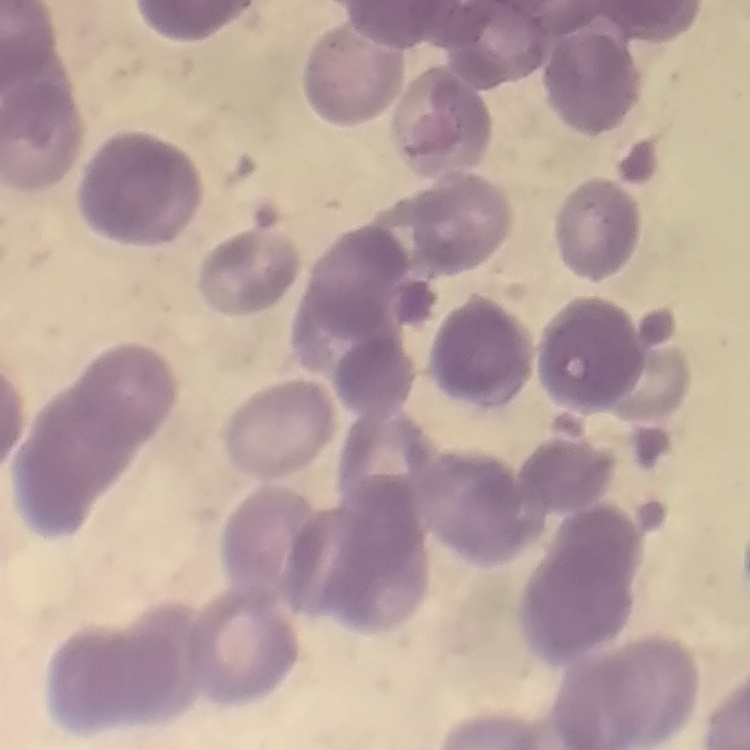

erythrocyte morphology = rouleaux formation
image type = one tile cut from a larger photomicrograph
stain = Field's or Giemsa
preparation = thin blood smear